Describe the morphology of the erythrocytes.
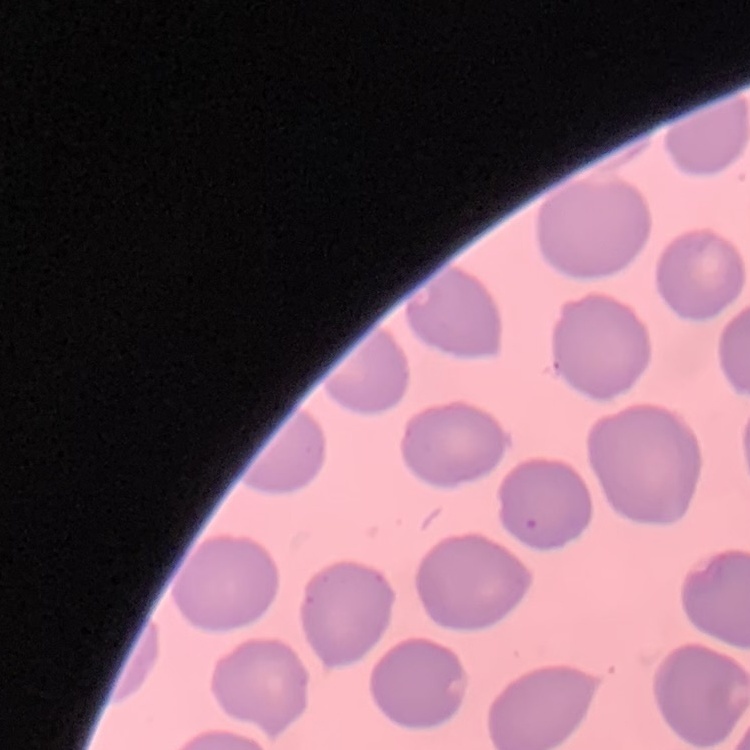
No rouleaux formation.

Summary:
  - Image type: square crop of a larger photomicrograph
  - Stain: Field's or Giemsa
  - Preparation: thin peripheral smear